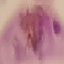

malaria status = parasitized
stain = Giemsa
image type = automatically extracted cell patch, resized to 64 × 64 pixels
capture = smartphone through the microscope eyepiece
preparation = thin blood film